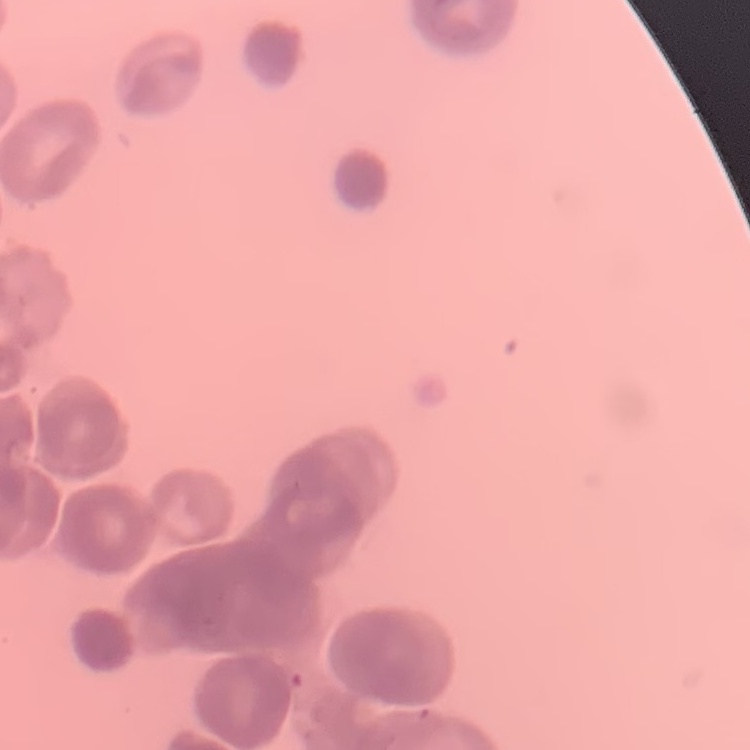

Summary:
  - Erythrocyte morphology: rouleaux formation
  - Image type: square crop of a larger photomicrograph
  - Preparation: thin blood film
  - Stain: Field's or Giemsa